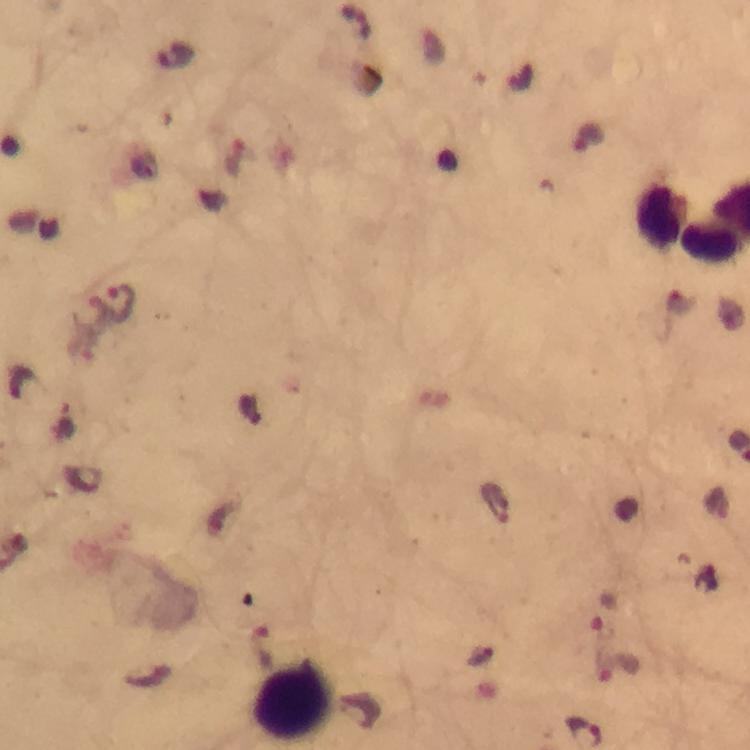
Approximate centers as (x, y) in pixels. Leukocyte locations: (295, 700). Plasmodium parasite locations: (355, 21), (119, 302). Immersion oil applied. Image is 750×750 pixels. Giemsa-stained preparation. Thick smear. From a malaria diagnostic workup. Photographed through the microscope with a smartphone camera. At 100x magnification. Cropped region of a single field of view.